Locate every blood parasite and identify its species.
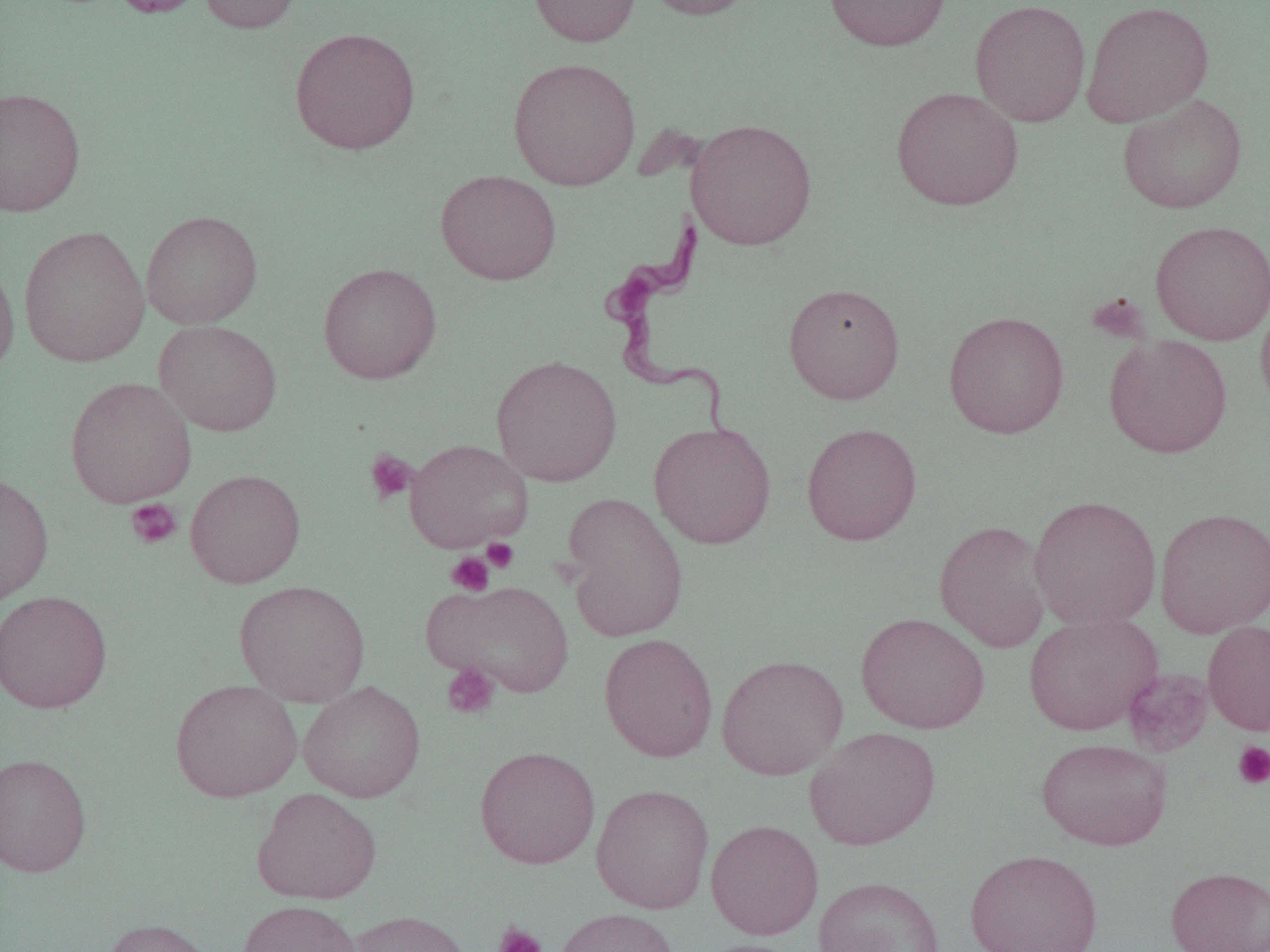
Approximate bounding boxes as (x1, y1, x2, y2) in pixels.
Trypanosoma brucei: (601, 205, 739, 451).
No Plasmodium falciparum, Plasmodium ovale, Plasmodium malariae, Plasmodium vivax, or Babesia divergens observed.

Platelet locations (subset): (1086, 292, 1150, 344), (364, 449, 416, 505), (126, 498, 182, 549), (481, 538, 519, 573), (445, 552, 495, 597), (442, 663, 500, 720), (1232, 741, 1270, 790), (493, 922, 547, 952). Uninfected red blood cell locations (subset): (108, 0, 208, 18), (198, 0, 304, 34), (528, 0, 640, 47), (639, 0, 758, 20), (824, 0, 950, 51), (970, 0, 1091, 127), (1081, 1, 1214, 127), (289, 27, 421, 155), (507, 57, 641, 190), (0, 86, 85, 216), (891, 87, 1023, 210), (1118, 93, 1247, 214), (686, 118, 817, 251), (435, 170, 561, 284), (141, 210, 263, 329), (1150, 220, 1270, 345), (18, 225, 151, 368), (0, 258, 20, 381), (318, 263, 441, 384), (783, 282, 905, 404), (1256, 296, 1270, 417), (943, 311, 1070, 439), (154, 320, 282, 436), (1103, 334, 1233, 458), (491, 354, 622, 487), (65, 376, 196, 508), (649, 422, 776, 549), (801, 422, 922, 546), (404, 438, 534, 552), (185, 469, 305, 588), (0, 472, 53, 606), (560, 492, 689, 642), (1027, 495, 1162, 631), (1155, 507, 1270, 637), (934, 519, 1052, 653), (426, 578, 575, 698), (234, 580, 371, 707), (0, 590, 113, 714), (856, 612, 990, 734), (1023, 613, 1163, 735), (1203, 620, 1270, 736), (599, 633, 718, 763), (716, 654, 848, 780), (170, 678, 303, 802), (298, 680, 425, 803), (804, 726, 941, 850), (1036, 737, 1173, 850), (474, 745, 600, 869), (0, 752, 91, 877), (591, 784, 714, 913), (252, 787, 381, 904), (705, 819, 824, 939), (965, 848, 1103, 952), (1166, 865, 1270, 952), (813, 877, 946, 952), (237, 900, 364, 952), (554, 907, 680, 952), (345, 909, 473, 952), (100, 917, 214, 952), (695, 939, 807, 952). Slide-level diagnosis: Trypanosoma brucei. Captured at 1000x magnification. Single field of view. Optical microscopy. Thin blood smear. Image is 1270×952 pixels.